Give the extent of all Plasmodium ovale-infected red blood cells.
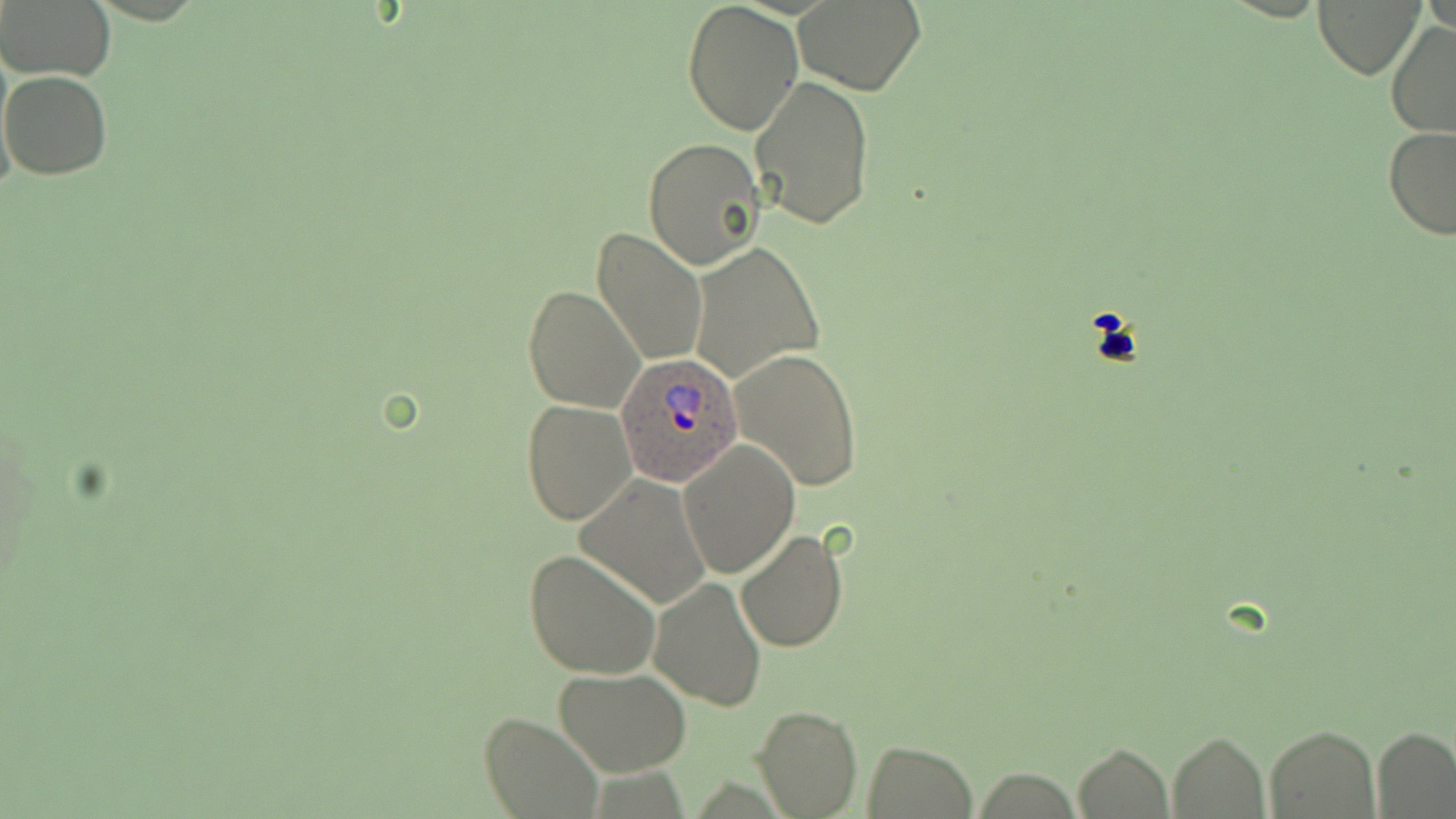
Approximate bounding boxes as named x1/y1/x2/y2 corners in pixels.
Plasmodium ovale-infected red blood cells: (x1=618, y1=353, x2=742, y2=486).

{
  "slide_level_diagnosis": "Plasmodium ovale",
  "uninfected_red_blood_cell_locations": "approximate bounding boxes as named x1/y1/x2/y2 corners in pixels: (x1=0, y1=0, x2=116, y2=83), (x1=793, y1=0, x2=925, y2=93), (x1=1315, y1=0, x2=1426, y2=79), (x1=681, y1=1, x2=803, y2=137), (x1=1385, y1=21, x2=1456, y2=141), (x1=1, y1=70, x2=114, y2=179), (x1=749, y1=75, x2=874, y2=231), (x1=1383, y1=124, x2=1456, y2=239), (x1=642, y1=138, x2=765, y2=268), (x1=590, y1=227, x2=709, y2=366), (x1=688, y1=243, x2=822, y2=383), (x1=521, y1=285, x2=645, y2=413), (x1=730, y1=348, x2=863, y2=492), (x1=521, y1=400, x2=636, y2=525), (x1=679, y1=439, x2=798, y2=578), (x1=576, y1=473, x2=713, y2=610), (x1=735, y1=528, x2=848, y2=653), (x1=523, y1=548, x2=661, y2=682), (x1=650, y1=578, x2=766, y2=710), (x1=554, y1=669, x2=693, y2=775), (x1=754, y1=705, x2=859, y2=816), (x1=478, y1=711, x2=601, y2=818), (x1=1264, y1=726, x2=1378, y2=817), (x1=1372, y1=728, x2=1456, y2=816), (x1=1167, y1=731, x2=1269, y2=816), (x1=862, y1=739, x2=977, y2=818), (x1=1073, y1=743, x2=1174, y2=819), (x1=971, y1=768, x2=1085, y2=817)",
  "image_size": "1456×819 pixels",
  "preparation": "thin blood smear",
  "field_of_view": "single",
  "stain": "May-Grünwald-Giemsa",
  "magnification": "1000x",
  "modality": "light microscopy"
}